Report the malaria status of this cell.
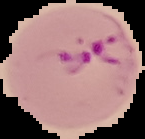
It is parasitized.

image type = cell region segmented out of the field of view; surrounding area masked to black
image size = 145×139 pixels
preparation = thin blood smear